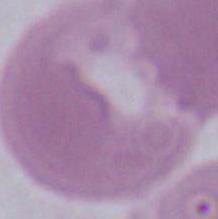

1000x magnification. A red blood cell is shown. Photomicrograph.